Locate every Plasmodium parasite.
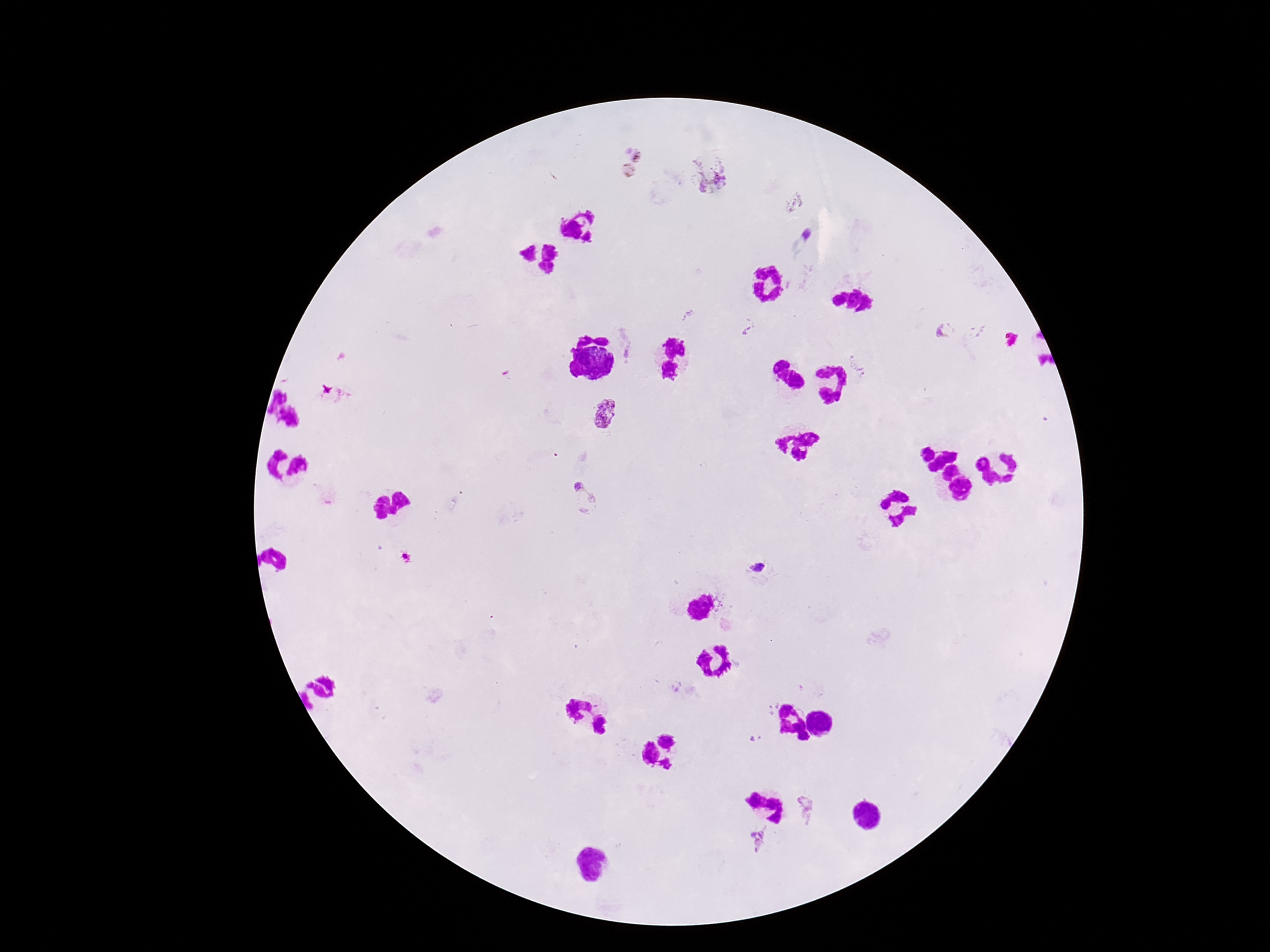

Approximate centers as {x, y} in pixels.
Plasmodium parasites: {629, 163}, {716, 183}, {807, 235}, {687, 315}, {747, 330}, {945, 331}, {860, 370}, {608, 414}, {587, 496}, {758, 567}, {805, 808}, {758, 842}.

Smartphone photograph taken through the microscope eyepiece. Giemsa-stained preparation. Patient malaria status: positive. 100x magnification. Image is 1270×952 pixels. One field from this slide. Thick peripheral-blood smear.